Give the position of every leukocyte visible.
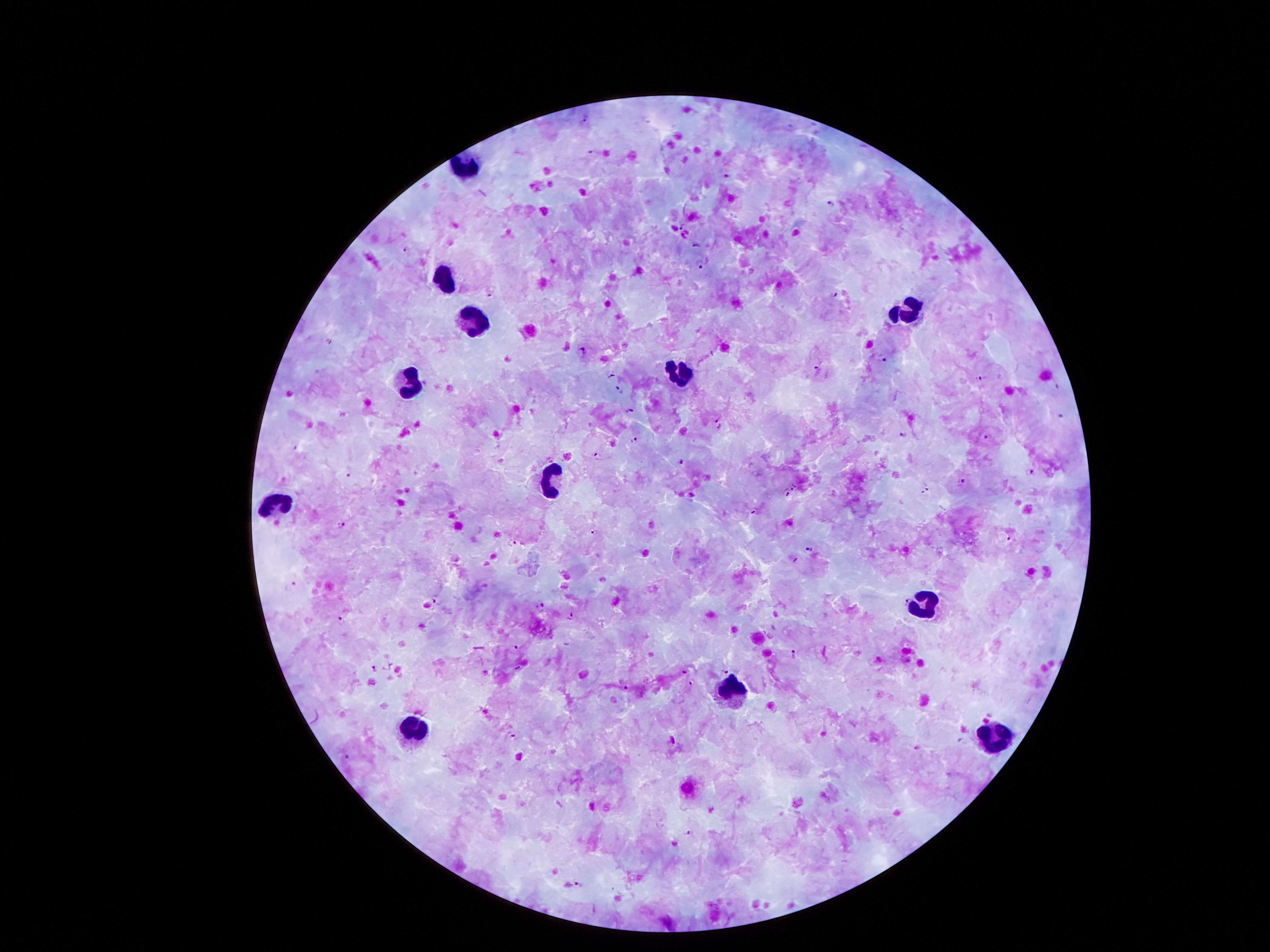
Approximate centers as [x, y] in pixels.
Leukocytes: [468, 164], [443, 276], [907, 311], [475, 324], [682, 374], [412, 385], [548, 475], [275, 498], [922, 605], [729, 689], [414, 729], [993, 740].

Summary:
  - Malaria parasite locations: [586, 122], [593, 152], [727, 175], [832, 205], [681, 227], [697, 245], [407, 248], [699, 264], [834, 295], [492, 296], [329, 342], [583, 351], [883, 358], [818, 371], [612, 375], [981, 377], [618, 389], [631, 411], [1063, 415], [718, 424], [904, 434], [987, 436], [636, 440], [295, 446], [597, 457], [681, 463], [1029, 471], [347, 474], [961, 481], [797, 487], [925, 488], [786, 493], [754, 510], [341, 522], [595, 532], [1009, 538], [511, 543], [811, 548], [292, 585], [905, 598], [437, 601], [540, 608], [570, 616], [342, 620], [512, 646], [794, 655], [685, 668], [372, 669], [725, 673], [694, 683], [626, 686], [516, 738], [916, 747], [349, 756], [688, 832], [578, 884]
  - Preparation: thick blood film
  - Magnification: 100x
  - Capture: smartphone through the microscope eyepiece
  - Field of view: one from this slide
  - Image size: 1270×952 pixels
  - Patient malaria status: infected with Plasmodium falciparum
  - Stain: Giemsa